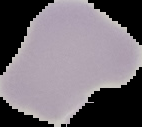

Summary:
  - Image size: 142×127 pixels
  - Malaria status: uninfected
  - Preparation: thin blood smear
  - Image type: segmented cell region on a black background